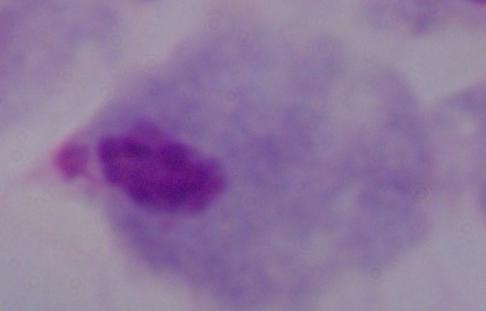
magnification: 1000x
identification: trichomonad
modality: photomicrograph